Give the position of every leukocyte visible.
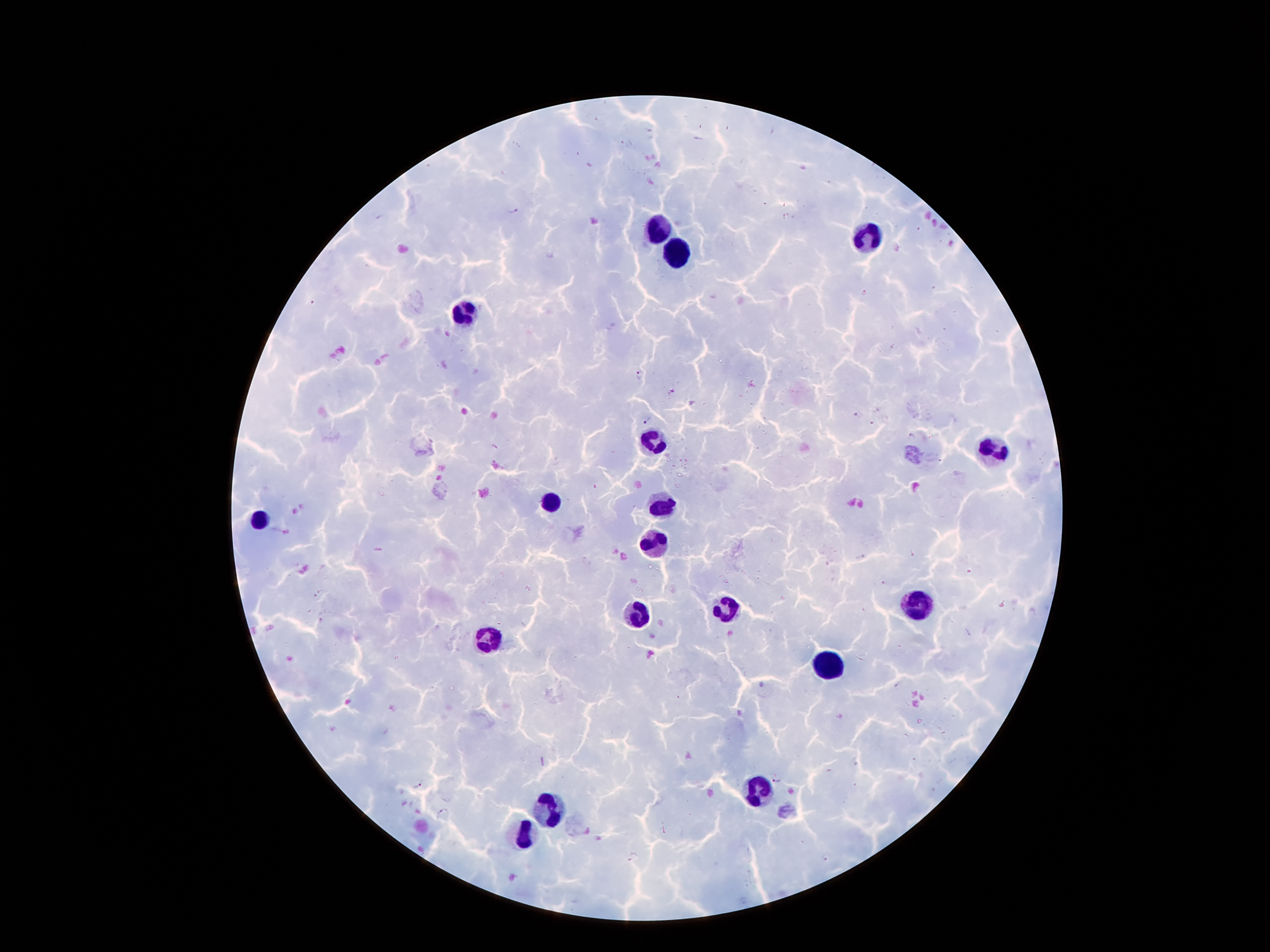
Approximate centers as [x, y] in pixels.
Leukocytes: [658, 231], [869, 237], [676, 253], [462, 310], [652, 442], [991, 448], [549, 500], [663, 505], [257, 521], [654, 541], [917, 602], [723, 610], [632, 613], [492, 640], [825, 665], [757, 790], [551, 809], [522, 833].

Summary:
  - Plasmodium parasite locations: [513, 211], [638, 375], [673, 391], [859, 414], [647, 419], [873, 425], [860, 558], [776, 778], [419, 784], [443, 812], [634, 858], [826, 858]
  - Patient malaria status: positive for Plasmodium falciparum
  - Magnification: 100x
  - Image size: 1270×952 pixels
  - Field of view: one from this slide
  - Stain: Giemsa
  - Capture: smartphone camera through the microscope eyepiece
  - Preparation: thick blood film